Classify this cell by malaria status.
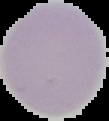

It is uninfected.

Summary:
  - Image type: segmented cell region on a black background
  - Image size: 109×121 pixels
  - Preparation: thin blood film